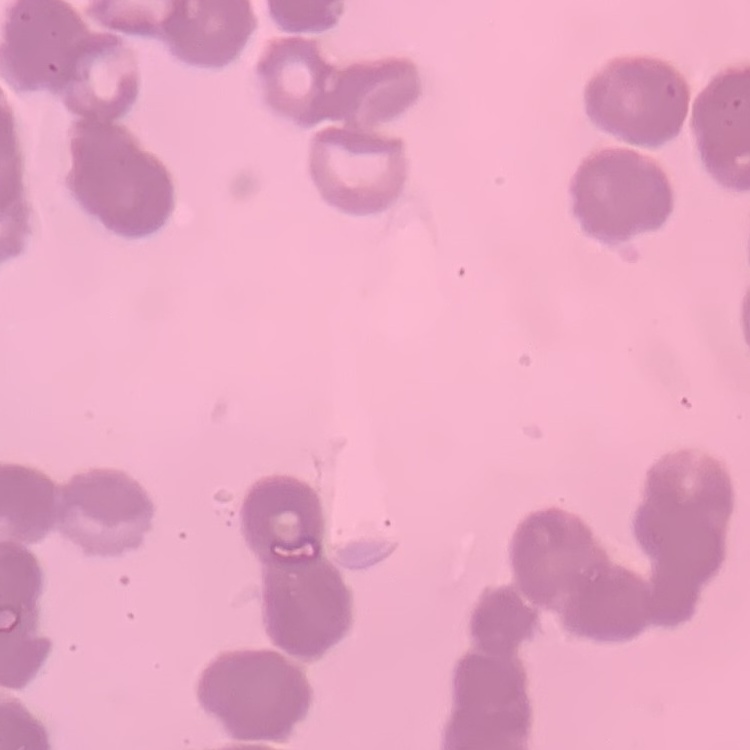
{
  "red_blood_cell_morphology": "rouleaux formation",
  "image_type": "one tile cut from a larger photomicrograph",
  "stain": "Field's or Giemsa",
  "preparation": "thin blood film"
}